Outline platelets.
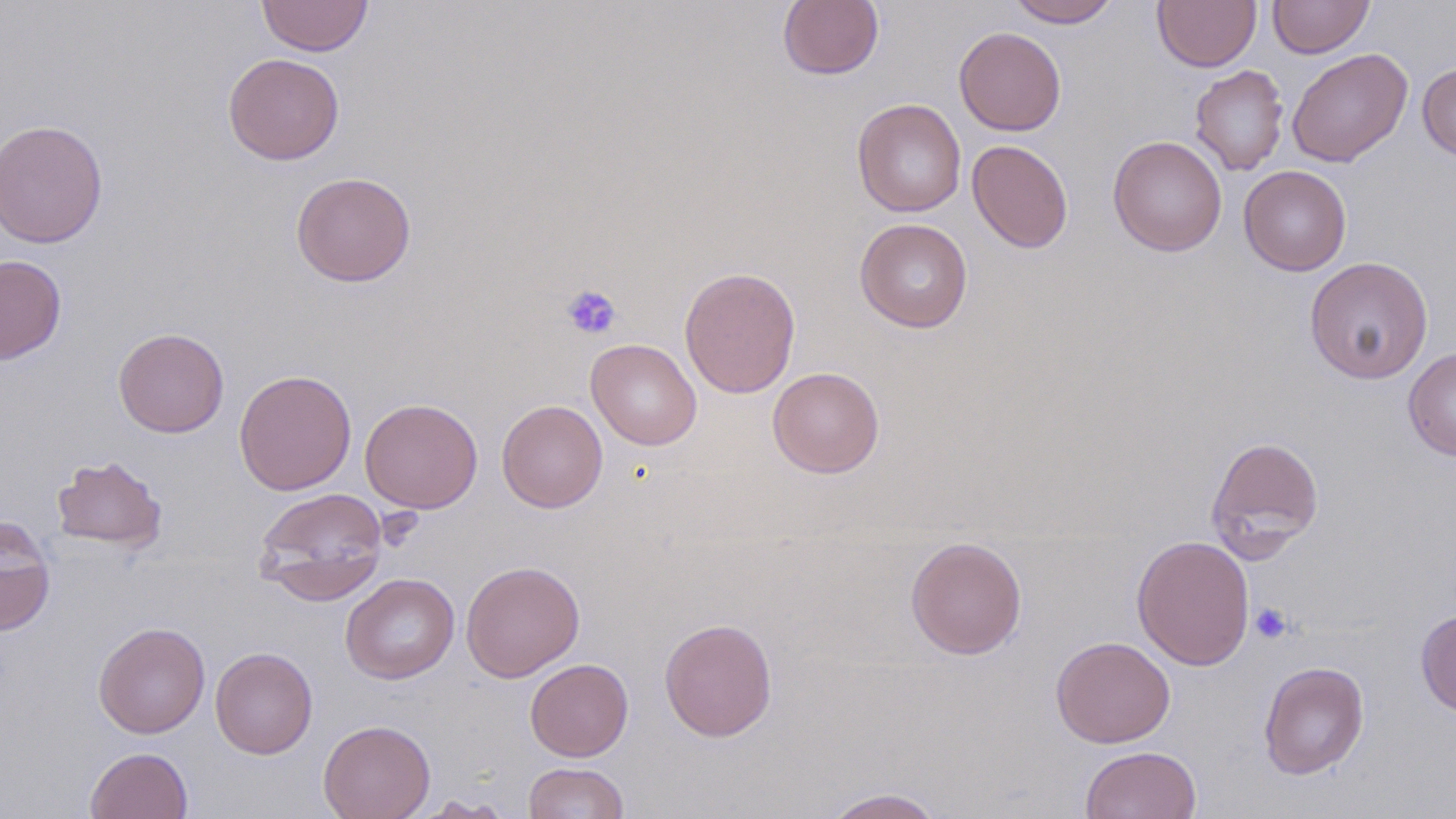
Approximate bounding boxes as (x1, y1, x2, y2) in pixels.
Platelets: (560, 284, 622, 341), (1250, 603, 1294, 644).

{
  "slide_level_diagnosis": "no evidence of blood parasites",
  "field_of_view": "one of a larger specimen",
  "preparation": "thin blood film",
  "magnification": "1000x",
  "uninfected_red_blood_cell_locations": "approximate bounding boxes as (x1, y1, x2, y2) in pixels: (256, 0, 374, 56), (778, 0, 883, 80), (1006, 0, 1121, 27), (1152, 0, 1261, 72), (1268, 0, 1374, 58), (954, 27, 1066, 135), (1286, 48, 1412, 167), (223, 52, 345, 165), (1417, 63, 1456, 161), (1189, 64, 1289, 176), (852, 98, 966, 217), (0, 119, 108, 248), (1108, 135, 1227, 256), (967, 139, 1073, 253), (1239, 165, 1351, 275), (290, 172, 416, 286), (854, 217, 973, 333), (0, 255, 67, 364), (1304, 256, 1433, 384), (680, 266, 801, 398), (113, 328, 230, 437), (587, 339, 702, 450), (1402, 347, 1456, 461), (768, 367, 885, 478), (234, 369, 357, 495), (359, 397, 483, 513), (496, 399, 608, 513), (1205, 436, 1325, 560), (51, 454, 167, 552), (253, 487, 388, 602), (0, 516, 55, 635), (1131, 534, 1255, 671), (905, 536, 1027, 660), (460, 560, 585, 682), (340, 573, 459, 683), (1415, 609, 1456, 718), (659, 617, 778, 742), (93, 622, 210, 738), (1050, 635, 1176, 748), (210, 646, 317, 758), (525, 658, 633, 761), (1258, 661, 1369, 780), (318, 719, 435, 819), (1080, 746, 1201, 819), (86, 747, 192, 819), (522, 762, 629, 819), (819, 787, 946, 818), (411, 796, 514, 818)",
  "modality": "light microscopy",
  "stain": "May-Grünwald-Giemsa",
  "image_size": "1456×819 pixels"
}